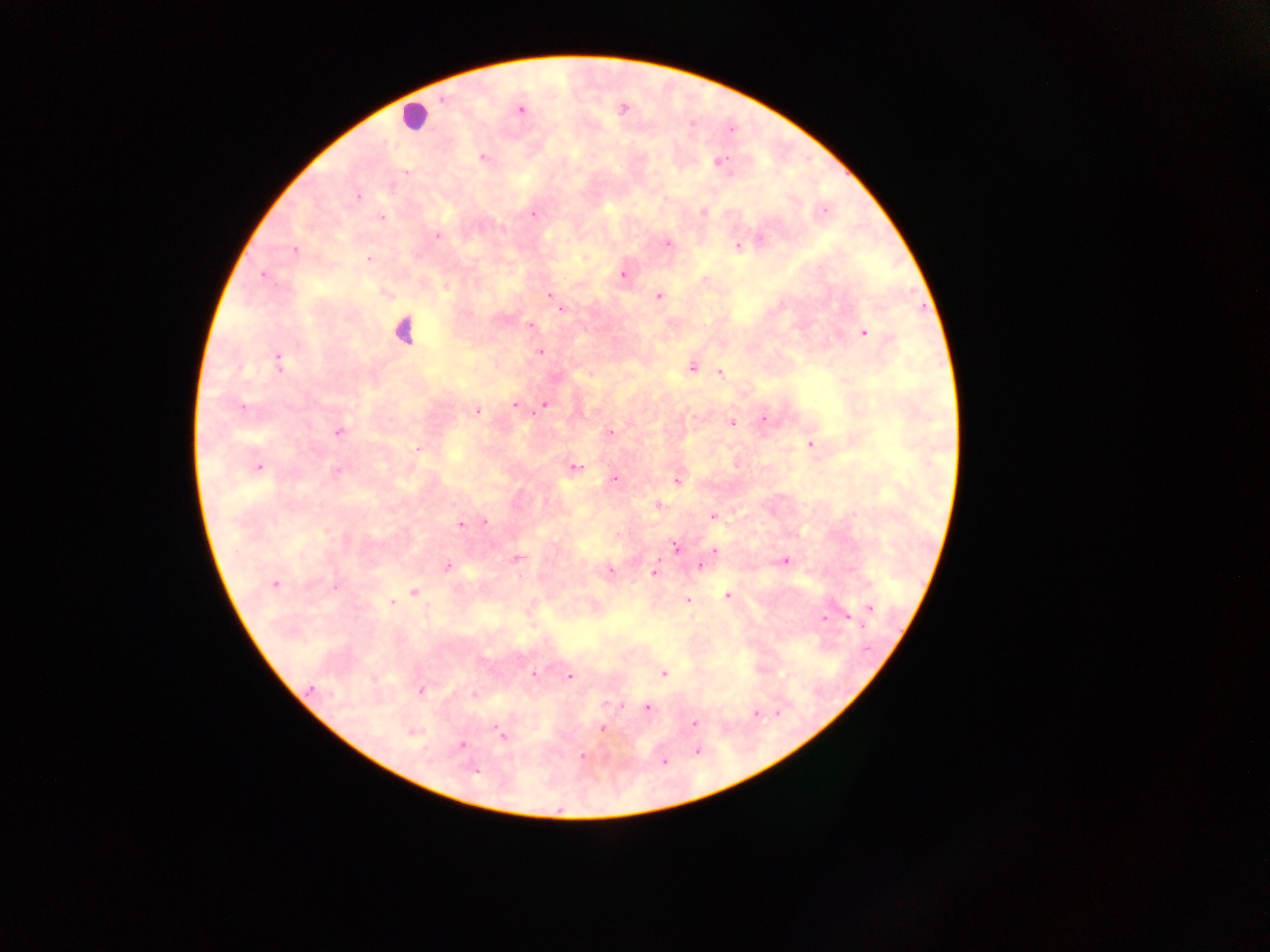

{
  "capture": "mobile-phone photograph through a microscope",
  "country": "Ghana",
  "leukocyte_locations": "approximate centers as (x, y) in pixels: (413, 116), (403, 331)",
  "preparation": "thick blood film",
  "malaria_parasite_locations": "approximate centers as (x, y) in pixels: (443, 99), (521, 109), (732, 130), (483, 157), (720, 160), (358, 197), (702, 212), (824, 212), (534, 215), (382, 218), (437, 236), (760, 239), (668, 244), (737, 246), (295, 250), (369, 259), (262, 274), (623, 274), (550, 294), (659, 296), (562, 309), (531, 325), (865, 333), (540, 352), (279, 362), (692, 368), (720, 373), (544, 404), (514, 405), (241, 407), (477, 411), (764, 419), (732, 423), (338, 432), (609, 433), (810, 445), (417, 450), (575, 467), (258, 468), (337, 471), (615, 479), (677, 482), (659, 505), (713, 516), (485, 521), (460, 525), (674, 546), (714, 551), (517, 558), (784, 561), (447, 566), (700, 566), (609, 570), (655, 572), (274, 584), (336, 587), (414, 592), (728, 596), (688, 601), (392, 602), (871, 609), (849, 617), (823, 618), (533, 673), (663, 673), (569, 676), (311, 689), (422, 690), (647, 707), (755, 714), (694, 723), (602, 729), (413, 733), (502, 735), (461, 745), (697, 751), (582, 756), (665, 761), (475, 771)",
  "image_size": "1270×952 pixels",
  "field_of_view": "single"
}